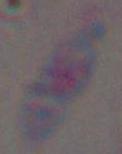

{
  "identification": "Toxoplasma gondii",
  "magnification": "1000x",
  "modality": "micrograph"
}